Report the malaria status of this cell.
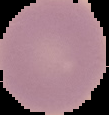
Uninfected.

Image is 109×115 pixels. The area outside the segmented cell region is set to black. From a thin blood smear.